Assess the morphology of the red blood cells.
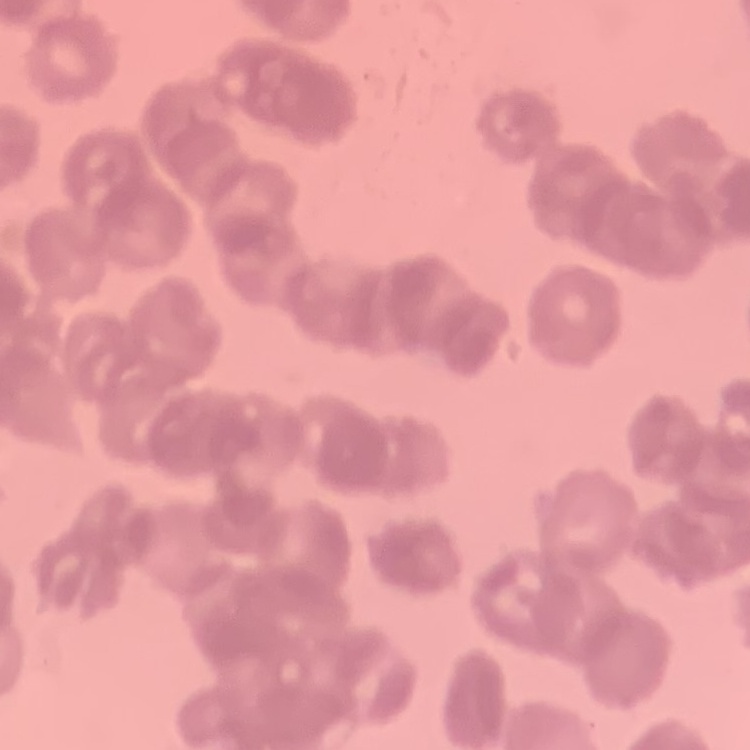

Rouleaux formation.

Stained with either Field's or Giemsa. Thin blood film. One tile cut from a larger photomicrograph.